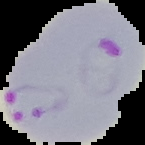
From a thin blood smear. Image is 145×145 pixels. Malaria status: parasitized. Segmented cell region on a black background.